Identify the blood parasite species.
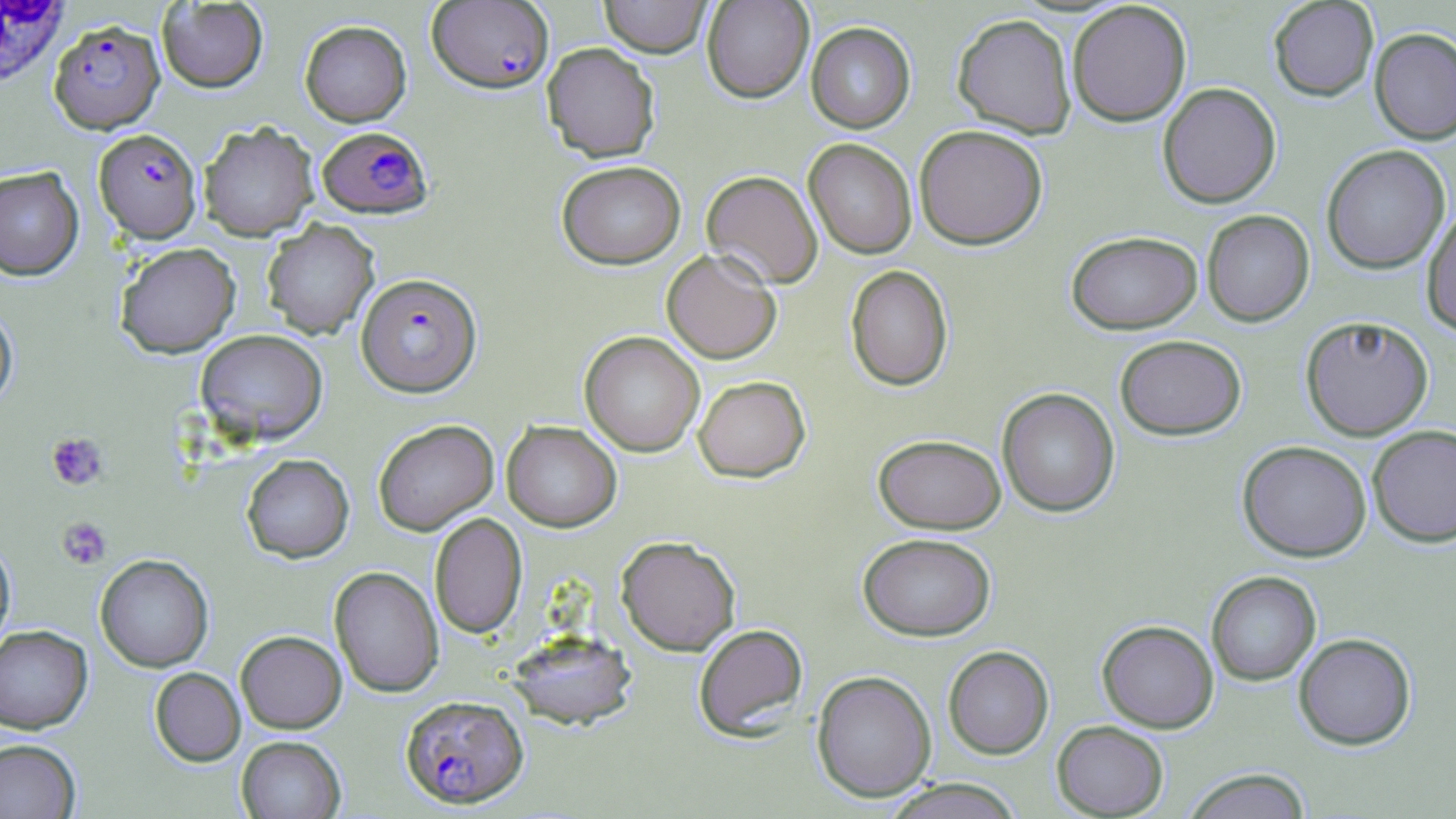

Plasmodium falciparum.

Summary:
  - Coordinate format: approximate bounding boxes as (x1, y1, x2, y2) in pixels
  - White blood cell locations: (0, 0, 69, 88)
  - Uninfected red blood cell locations: (598, 0, 713, 58), (701, 0, 814, 103), (1268, 0, 1379, 101), (157, 1, 268, 93), (1067, 1, 1192, 126), (952, 13, 1077, 139), (300, 20, 411, 127), (805, 21, 915, 133), (1369, 27, 1456, 145), (542, 42, 661, 162), (1157, 82, 1281, 208), (198, 122, 319, 240), (914, 124, 1048, 250), (803, 138, 917, 259), (1321, 144, 1450, 274), (557, 160, 686, 269), (0, 166, 84, 280), (701, 170, 823, 289), (1422, 203, 1456, 337), (1202, 209, 1314, 326), (261, 218, 380, 339), (1066, 230, 1203, 334), (115, 242, 240, 358), (661, 248, 782, 364), (845, 264, 953, 391), (0, 302, 18, 413), (1300, 315, 1434, 440), (195, 329, 328, 444), (579, 331, 705, 457), (1114, 334, 1247, 440), (693, 375, 810, 482), (997, 388, 1120, 517), (373, 419, 498, 536), (502, 421, 622, 531), (1367, 424, 1456, 548), (873, 434, 1006, 534), (1237, 440, 1372, 562), (241, 454, 354, 562), (429, 512, 527, 638), (857, 532, 996, 641), (615, 535, 741, 656), (0, 537, 16, 656), (95, 554, 214, 672), (329, 566, 444, 697), (1206, 571, 1321, 686), (1097, 620, 1219, 733), (693, 623, 809, 740), (0, 625, 93, 734), (507, 629, 638, 730), (235, 630, 347, 733), (1293, 632, 1416, 750), (943, 646, 1054, 760), (149, 667, 246, 766), (811, 670, 936, 802), (1052, 720, 1169, 818), (236, 735, 346, 819), (0, 738, 81, 819), (1181, 768, 1313, 819), (881, 778, 1025, 818)
  - Plasmodium falciparum-infected red blood cell locations: (427, 1, 554, 93), (49, 18, 164, 133), (317, 126, 433, 218), (94, 129, 202, 243), (356, 272, 482, 397), (401, 693, 528, 808)
  - Platelet locations: (45, 431, 109, 491), (57, 517, 111, 569)
  - Field of view: single
  - Image size: 1456×819 pixels
  - Magnification: 1000x
  - Modality: light microscopy
  - Preparation: thin blood smear
  - Stain: May-Grünwald-Giemsa